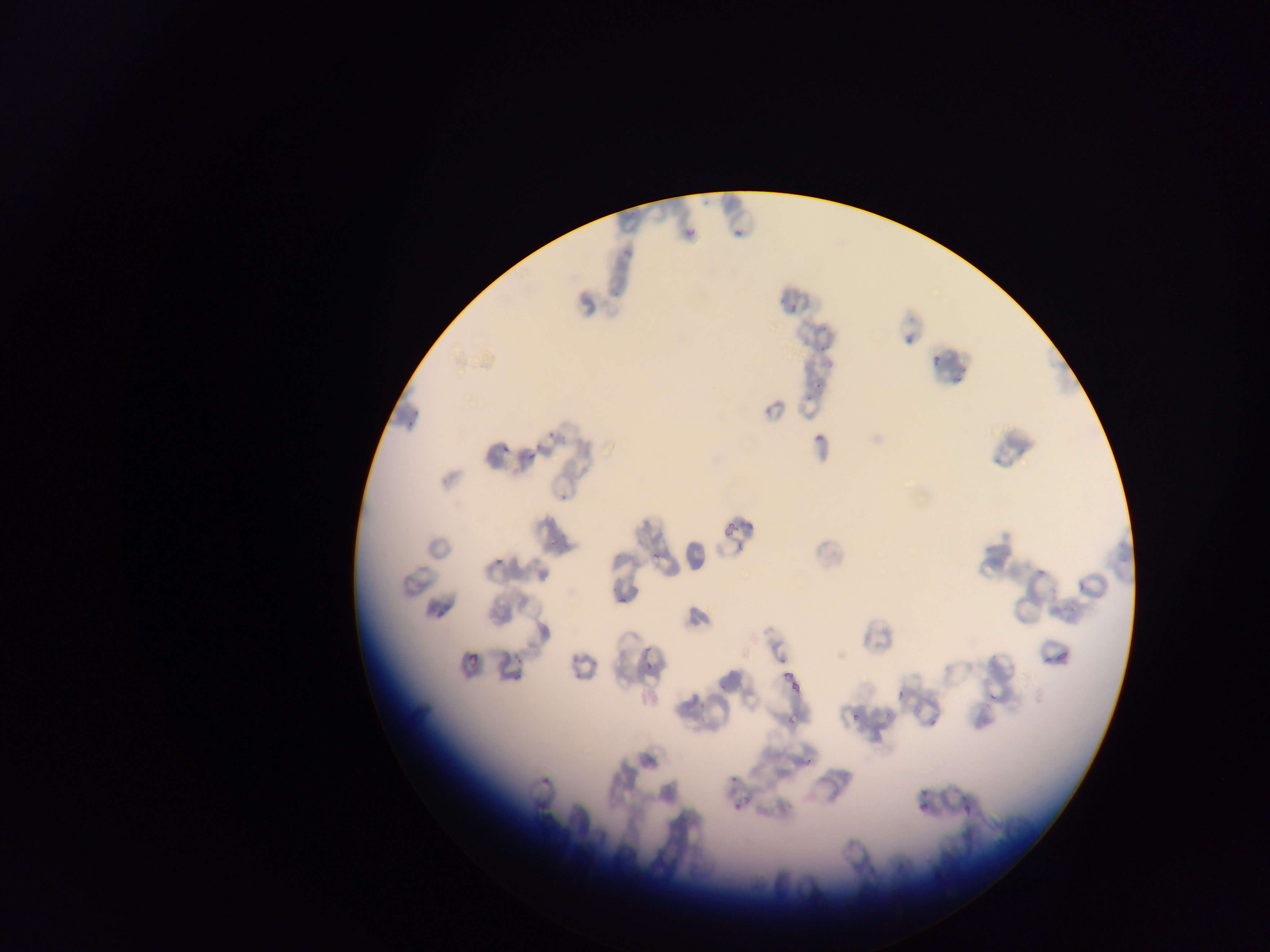
field of view = single
preparation = thin blood film
capture = mobile-phone photograph through a microscope
image size = 1270×952 pixels
Plasmodium parasite locations = approximate bounding boxes as [left, top, right, bottom] in pixels: [733, 228, 743, 237], [686, 229, 696, 239], [790, 304, 798, 313], [932, 355, 942, 365], [815, 433, 824, 443], [499, 444, 511, 455], [525, 448, 537, 462], [651, 551, 662, 562], [493, 557, 504, 567], [618, 595, 627, 605], [1055, 645, 1072, 665], [467, 651, 479, 665], [643, 663, 653, 673], [774, 669, 798, 682], [896, 675, 914, 700], [788, 681, 809, 699], [849, 711, 860, 722], [784, 713, 801, 723], [928, 719, 937, 728], [540, 776, 551, 787], [961, 794, 978, 815], [735, 796, 750, 811], [914, 803, 926, 817]
country = Ghana